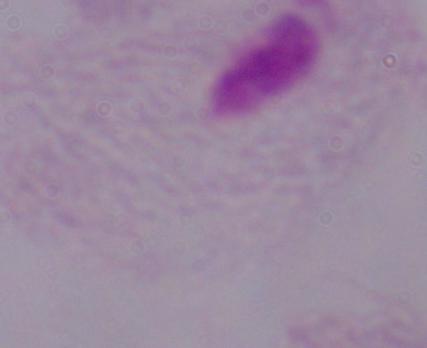

magnification = 1000x
identification = trichomonad
modality = photomicrograph